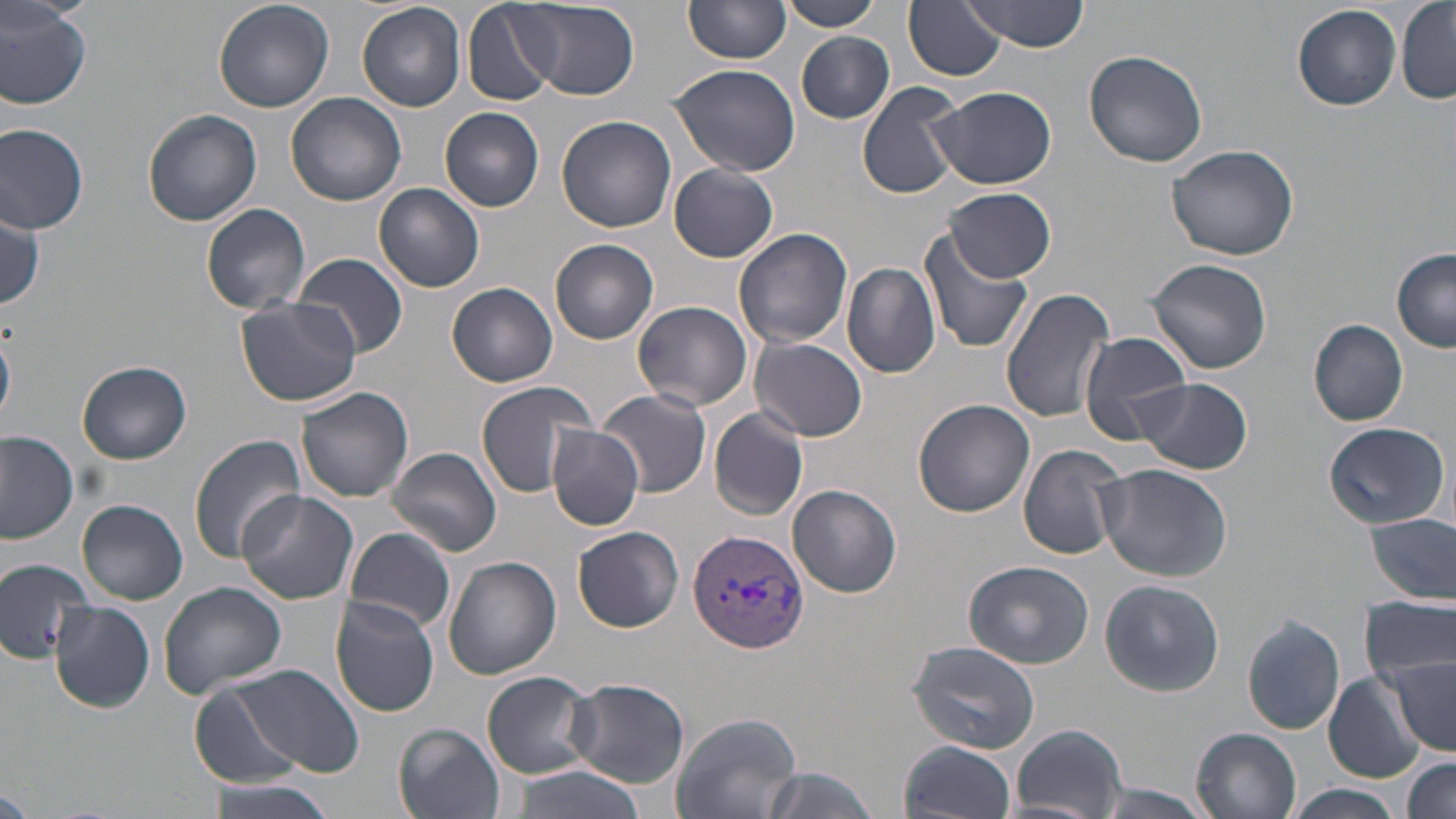 Approximate bounding boxes as (x1,y1)-(x2,y2) corner pairs in pixels. Plasmodium vivax-infected red blood cell locations: (689,528)-(810,652). Uninfected red blood cell locations: (214,0)-(335,114), (775,0)-(883,31), (903,0)-(1007,82), (515,1)-(640,100), (962,1)-(1091,52), (1396,1)-(1456,105), (0,2)-(91,111), (356,2)-(466,112), (461,2)-(558,107), (684,2)-(791,66), (1292,3)-(1401,111), (796,31)-(894,124), (1084,50)-(1209,168), (668,62)-(801,176), (856,81)-(966,200), (929,86)-(1058,190), (286,93)-(408,207), (440,108)-(544,212), (143,109)-(263,225), (557,115)-(678,233), (0,123)-(89,234), (1167,144)-(1299,260), (669,164)-(778,263), (375,182)-(485,292), (945,186)-(1055,283), (201,204)-(311,314), (0,205)-(46,310), (733,227)-(852,349), (918,228)-(1034,355), (550,238)-(659,344), (1392,250)-(1456,352), (294,253)-(408,357), (1146,255)-(1274,375), (842,263)-(940,379), (447,282)-(558,387), (1001,284)-(1118,424), (235,296)-(362,408), (634,300)-(752,412), (1308,319)-(1408,426), (1078,330)-(1194,444), (750,336)-(871,441), (77,359)-(191,465), (1134,377)-(1253,474), (475,381)-(596,498), (295,386)-(415,503), (597,390)-(713,497), (913,399)-(1034,515), (709,408)-(808,521), (1321,422)-(1451,530), (545,424)-(645,530), (0,432)-(80,544), (188,434)-(308,562), (1018,445)-(1128,559), (389,447)-(501,558), (1094,463)-(1233,581), (788,484)-(902,599), (236,491)-(359,604), (77,499)-(189,605), (1364,513)-(1455,604), (344,526)-(455,635), (573,527)-(683,631), (443,556)-(562,680), (0,557)-(97,666), (965,561)-(1095,669), (1098,578)-(1224,697), (157,582)-(287,698), (329,596)-(441,717), (1362,596)-(1453,684), (50,600)-(154,715), (1242,616)-(1345,735), (908,639)-(1045,754), (1386,659)-(1455,757), (236,664)-(365,778), (482,672)-(596,778), (1322,672)-(1427,782), (565,678)-(690,786), (190,682)-(301,789), (673,712)-(802,819), (393,724)-(505,819), (1008,725)-(1130,817), (1190,726)-(1303,819), (898,740)-(1017,819), (1401,757)-(1455,817), (503,763)-(645,819), (752,766)-(882,819), (199,775)-(341,819), (1079,782)-(1222,819), (0,784)-(33,816), (1288,784)-(1405,818). Slide-level diagnosis: Plasmodium vivax. One field of a larger specimen. Light microscopy. Image is 1456×819 pixels. Captured at 1000x magnification. Thin blood smear. May-Grünwald-Giemsa-stained preparation.